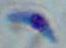
Summary:
  - Identification: Toxoplasma gondii
  - Modality: micrograph
  - Magnification: 1000x